Assess this cell for malaria.
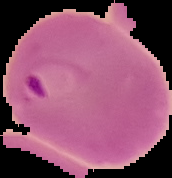

It is parasitized.

Summary:
  - Image size: 172×178 pixels
  - Preparation: thin blood film
  - Image type: segmented cell region with the area outside set to black